Assess this cell for malaria.
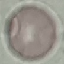
It is uninfected.

{
  "stain": "Giemsa",
  "image_type": "cell patch, automatically extracted from a larger field of view and resized to 64 × 64 pixels",
  "preparation": "thin blood smear",
  "capture": "smartphone through the microscope eyepiece"
}